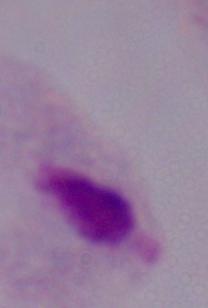

Micrograph. 1000x magnification. A trichomonad is seen.